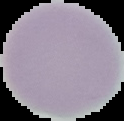
Summary:
  - Preparation: thin blood smear
  - Image size: 124×121 pixels
  - Image type: segmented cell region with the area outside set to black
  - Result: no malaria parasites seen